State which cell type is depicted.
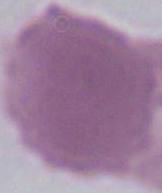
An erythrocyte.

Micrograph. 1000x magnification.